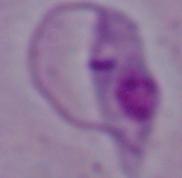

A Leishmania parasite is seen. Micrograph. 1000x magnification.